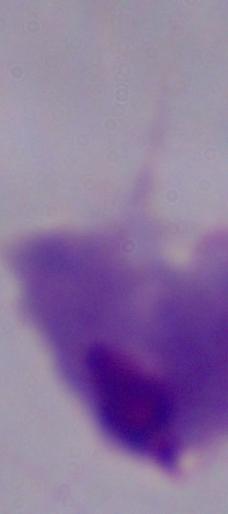
modality: micrograph
identification: trichomonad
magnification: 1000x